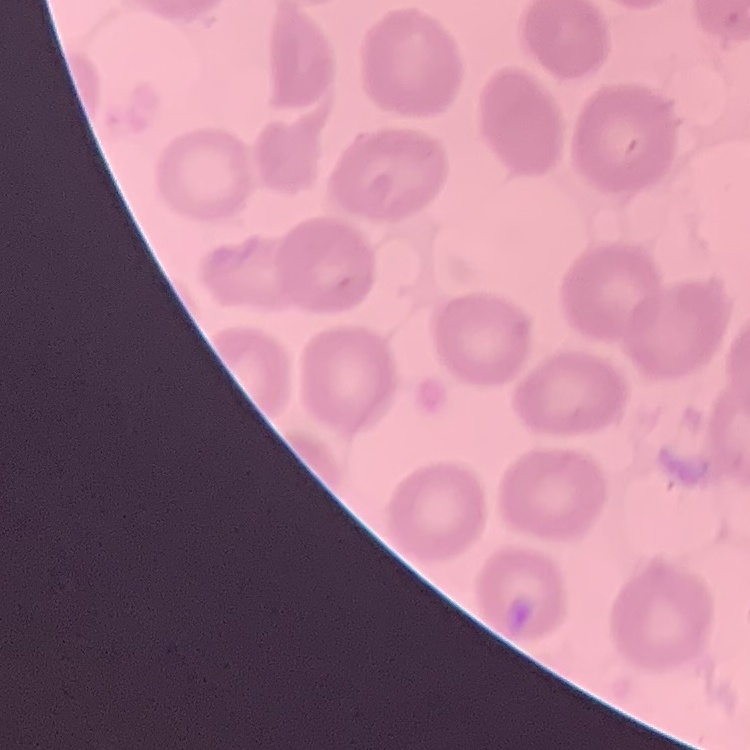 The red blood cells exhibit no rouleaux formation. Thin blood film. Square crop of a larger photomicrograph. Stained with either Field's or Giemsa.